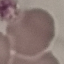

{
  "malaria_status": "uninfected",
  "stain": "Giemsa",
  "image_type": "cell patch, automatically extracted from a larger field of view and resized to 64 × 64 pixels",
  "preparation": "thin blood smear",
  "capture": "smartphone camera at the microscope eyepiece"
}